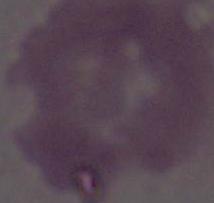 Micrograph. Captured at 1000x magnification. An erythrocyte is shown.